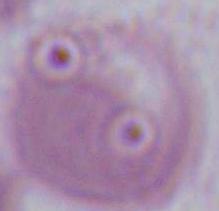

Summary:
  - Magnification: 1000x
  - Modality: micrograph
  - Identification: red blood cell